Comment on the morphology of the red blood cells.
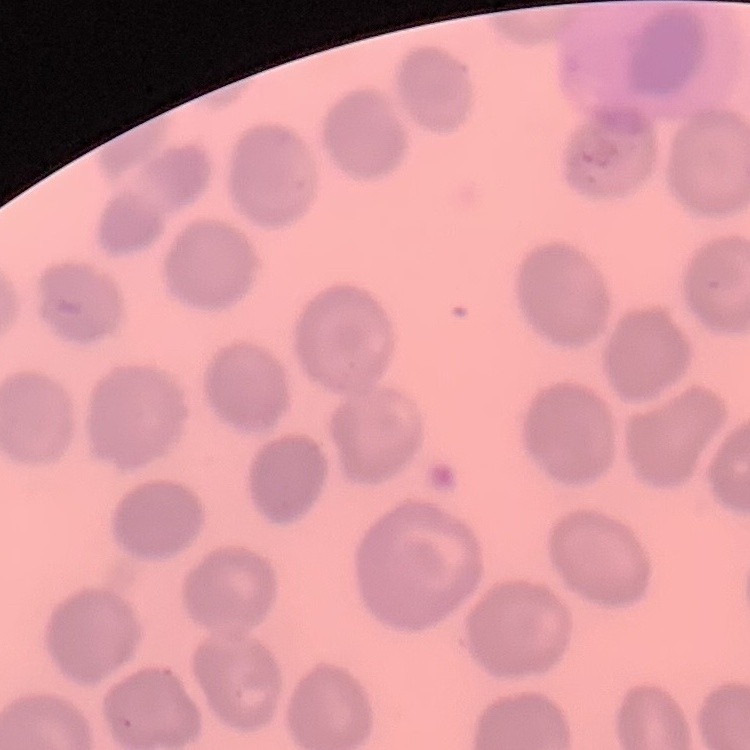
No rouleaux formation.

preparation = thin peripheral smear
stain = Field's or Giemsa
image type = one tile cut from a larger photomicrograph